Describe the morphology of the red blood cells.
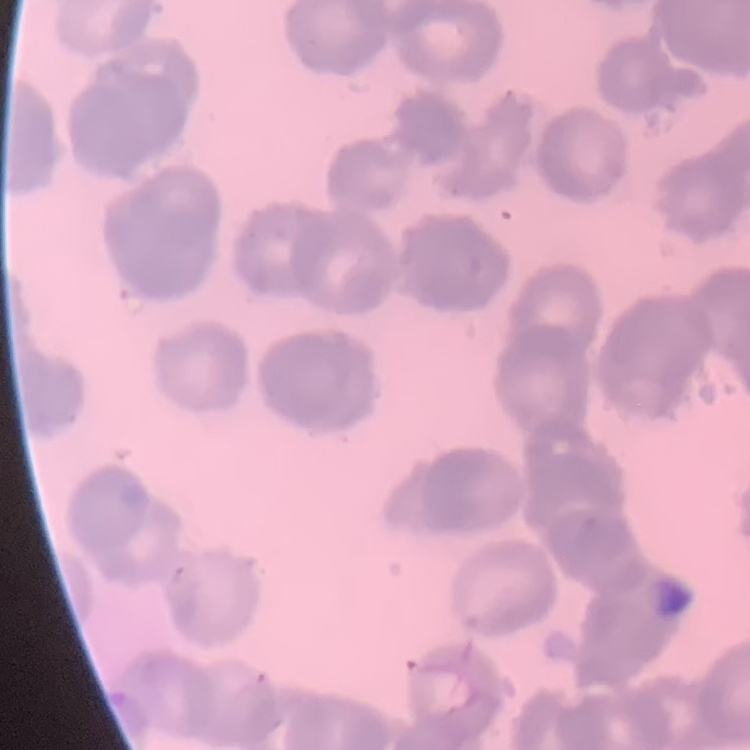

They show rouleaux formation.

preparation = thin blood smear
image type = one tile cut from a larger photomicrograph
stain = Field's or Giemsa